Name the blood parasite species.
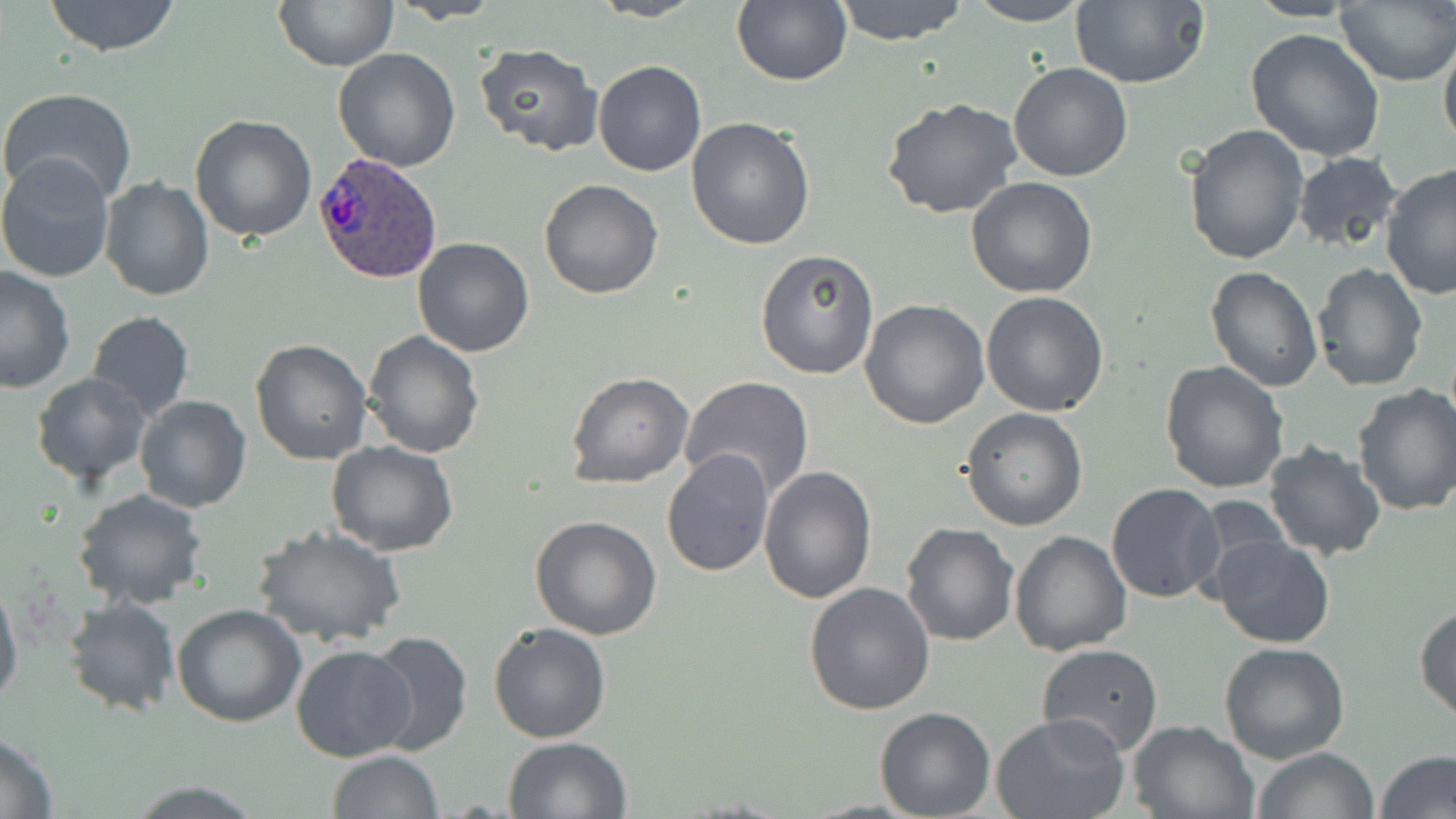
Plasmodium ovale.

Approximate bounding boxes as named x1/y1/x2/y2 corners in pixels. Plasmodium ovale-infected red blood cell locations: (x1=314, y1=151, x2=442, y2=284). Uninfected red blood cell locations: (x1=43, y1=0, x2=183, y2=56), (x1=589, y1=0, x2=707, y2=23), (x1=732, y1=0, x2=852, y2=86), (x1=832, y1=0, x2=969, y2=45), (x1=963, y1=0, x2=1093, y2=26), (x1=1069, y1=0, x2=1209, y2=89), (x1=273, y1=1, x2=399, y2=70), (x1=390, y1=1, x2=504, y2=23), (x1=1336, y1=2, x2=1456, y2=86), (x1=1244, y1=27, x2=1388, y2=161), (x1=1439, y1=31, x2=1456, y2=159), (x1=473, y1=43, x2=603, y2=155), (x1=332, y1=48, x2=461, y2=171), (x1=592, y1=61, x2=707, y2=178), (x1=1007, y1=62, x2=1134, y2=183), (x1=1, y1=87, x2=138, y2=207), (x1=881, y1=97, x2=1025, y2=221), (x1=188, y1=114, x2=317, y2=243), (x1=687, y1=116, x2=816, y2=250), (x1=1184, y1=125, x2=1310, y2=267), (x1=0, y1=151, x2=117, y2=284), (x1=1291, y1=152, x2=1404, y2=257), (x1=1379, y1=163, x2=1455, y2=300), (x1=965, y1=175, x2=1098, y2=298), (x1=100, y1=176, x2=214, y2=301), (x1=539, y1=179, x2=665, y2=299), (x1=411, y1=237, x2=536, y2=357), (x1=755, y1=247, x2=879, y2=380), (x1=1311, y1=261, x2=1429, y2=392), (x1=0, y1=265, x2=78, y2=394), (x1=1205, y1=266, x2=1322, y2=392), (x1=981, y1=291, x2=1109, y2=415), (x1=859, y1=298, x2=989, y2=430), (x1=86, y1=311, x2=195, y2=422), (x1=363, y1=331, x2=485, y2=459), (x1=250, y1=338, x2=374, y2=465), (x1=1158, y1=360, x2=1289, y2=494), (x1=567, y1=372, x2=694, y2=488), (x1=31, y1=373, x2=152, y2=486), (x1=680, y1=376, x2=816, y2=500), (x1=1351, y1=383, x2=1456, y2=518), (x1=134, y1=394, x2=252, y2=512), (x1=961, y1=409, x2=1087, y2=530), (x1=324, y1=439, x2=458, y2=556), (x1=1262, y1=439, x2=1387, y2=561), (x1=662, y1=449, x2=774, y2=576), (x1=759, y1=466, x2=877, y2=604), (x1=1106, y1=483, x2=1226, y2=604), (x1=70, y1=489, x2=209, y2=609), (x1=531, y1=516, x2=663, y2=640), (x1=900, y1=522, x2=1019, y2=646), (x1=253, y1=523, x2=406, y2=647), (x1=1008, y1=531, x2=1132, y2=656), (x1=1209, y1=534, x2=1335, y2=649), (x1=0, y1=576, x2=22, y2=714), (x1=804, y1=583, x2=936, y2=717), (x1=63, y1=597, x2=180, y2=716), (x1=171, y1=603, x2=306, y2=727), (x1=1414, y1=604, x2=1456, y2=726), (x1=487, y1=622, x2=611, y2=743), (x1=365, y1=631, x2=474, y2=756), (x1=1219, y1=643, x2=1350, y2=765), (x1=290, y1=644, x2=417, y2=763), (x1=1036, y1=644, x2=1164, y2=757), (x1=874, y1=707, x2=996, y2=819), (x1=992, y1=713, x2=1132, y2=819), (x1=1127, y1=718, x2=1258, y2=818), (x1=0, y1=733, x2=59, y2=816), (x1=502, y1=736, x2=632, y2=818), (x1=1250, y1=746, x2=1380, y2=819), (x1=326, y1=750, x2=442, y2=818), (x1=1376, y1=751, x2=1456, y2=819), (x1=125, y1=780, x2=265, y2=816). One field of a larger specimen. Optical microscopy. Image is 1456×819 pixels. 1000x magnification. Thin blood smear. May-Grünwald-Giemsa-stained preparation.